State which parasite is depicted.
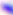
This is Toxoplasma gondii.

Summary:
  - Modality: micrograph
  - Magnification: 400x